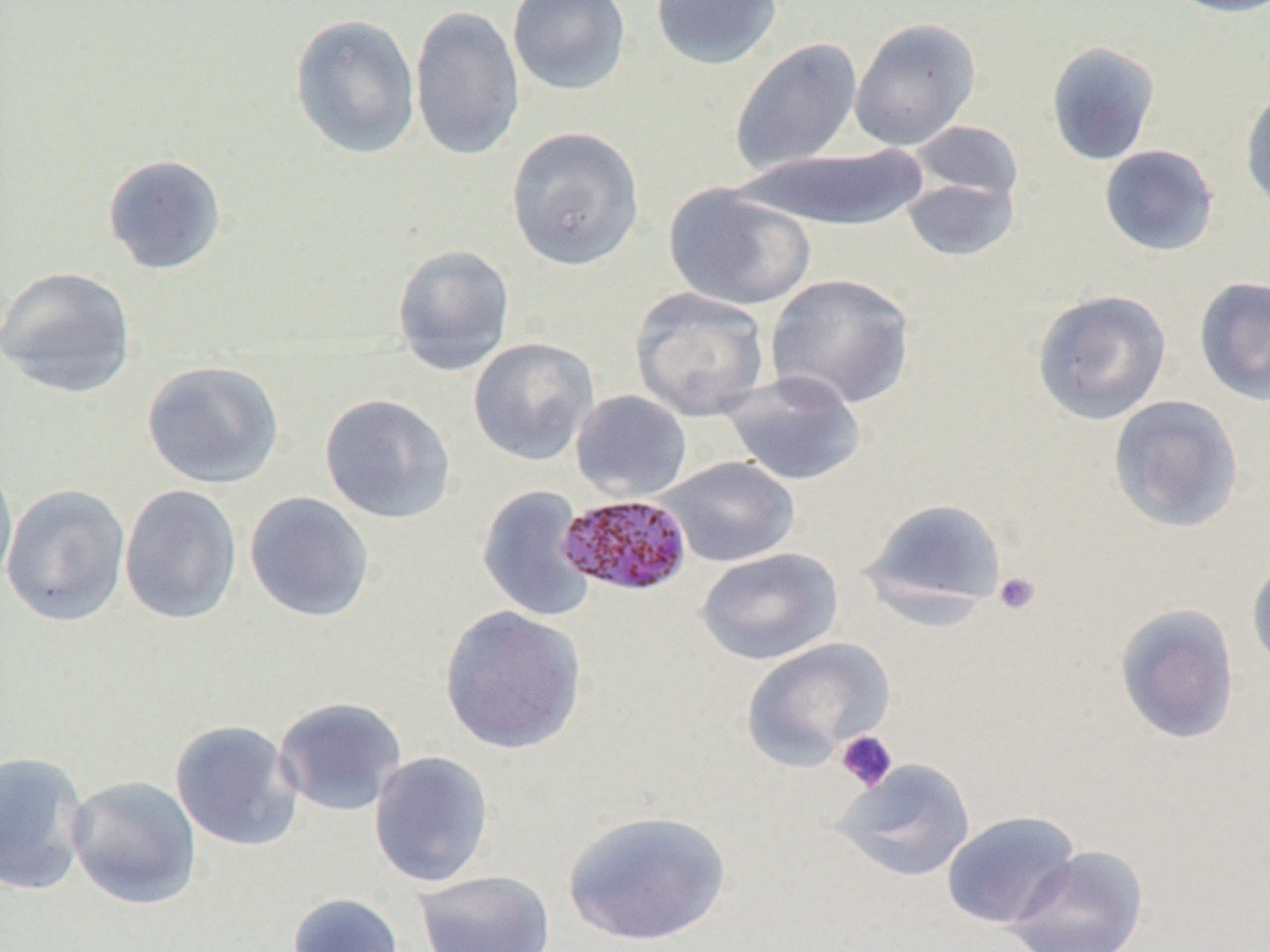

Summary:
  - Coordinate format: approximate bounding boxes as named x1/y1/x2/y2 corners in pixels
  - Platelet locations: (x1=992, y1=571, x2=1042, y2=616), (x1=835, y1=730, x2=898, y2=793)
  - Uninfected red blood cell locations (subset): (x1=507, y1=0, x2=632, y2=96), (x1=650, y1=0, x2=783, y2=71), (x1=1162, y1=0, x2=1270, y2=19), (x1=409, y1=5, x2=526, y2=161), (x1=289, y1=14, x2=421, y2=160), (x1=849, y1=17, x2=981, y2=151), (x1=728, y1=37, x2=863, y2=177), (x1=1045, y1=41, x2=1161, y2=166), (x1=1239, y1=85, x2=1270, y2=218), (x1=906, y1=119, x2=1024, y2=207), (x1=506, y1=126, x2=645, y2=271), (x1=1098, y1=144, x2=1219, y2=257), (x1=738, y1=145, x2=934, y2=233), (x1=102, y1=154, x2=227, y2=276), (x1=901, y1=176, x2=1019, y2=263), (x1=664, y1=183, x2=816, y2=311), (x1=392, y1=244, x2=516, y2=377), (x1=1, y1=266, x2=137, y2=398), (x1=764, y1=273, x2=916, y2=410), (x1=1194, y1=276, x2=1270, y2=406), (x1=631, y1=287, x2=771, y2=421), (x1=1031, y1=289, x2=1172, y2=425), (x1=468, y1=336, x2=599, y2=466), (x1=141, y1=359, x2=284, y2=489), (x1=722, y1=371, x2=868, y2=487), (x1=570, y1=390, x2=692, y2=502), (x1=318, y1=393, x2=457, y2=525), (x1=1108, y1=395, x2=1245, y2=534), (x1=658, y1=456, x2=799, y2=567), (x1=0, y1=461, x2=18, y2=596), (x1=1, y1=484, x2=131, y2=626), (x1=118, y1=484, x2=242, y2=626), (x1=476, y1=485, x2=596, y2=623), (x1=244, y1=491, x2=375, y2=623), (x1=859, y1=497, x2=1009, y2=618), (x1=695, y1=548, x2=843, y2=665), (x1=1246, y1=550, x2=1270, y2=676), (x1=1114, y1=603, x2=1240, y2=745), (x1=438, y1=605, x2=587, y2=756), (x1=741, y1=637, x2=895, y2=771), (x1=273, y1=696, x2=407, y2=817), (x1=170, y1=719, x2=303, y2=852), (x1=0, y1=750, x2=90, y2=896), (x1=368, y1=751, x2=495, y2=888), (x1=831, y1=758, x2=976, y2=882), (x1=66, y1=775, x2=203, y2=910), (x1=562, y1=809, x2=731, y2=947), (x1=940, y1=810, x2=1081, y2=929), (x1=1003, y1=845, x2=1149, y2=951), (x1=413, y1=870, x2=557, y2=952), (x1=287, y1=892, x2=404, y2=952)
  - Slide-level diagnosis: Plasmodium malariae
  - Magnification: 1000x
  - Modality: light microscopy
  - Image size: 1270×952 pixels
  - Field of view: one of a larger specimen
  - Preparation: thin blood smear